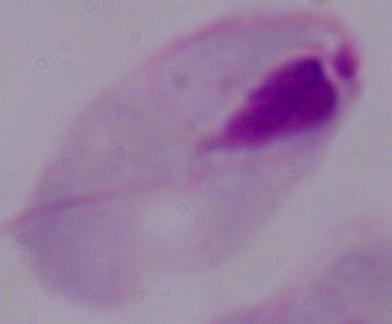

Summary:
  - Magnification: 1000x
  - Modality: micrograph
  - Identification: trichomonad